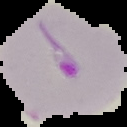
result = Plasmodium parasites identified
image size = 127×127 pixels
image type = cell region segmented out of the field of view; surrounding area masked to black
preparation = thin blood film